Classify this cell by malaria status.
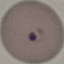

It is parasitized.

Thin blood film. Automatically extracted cell patch, resized to 64 × 64 pixels. Photographed with a smartphone camera at the microscope eyepiece. Giemsa-stained preparation.